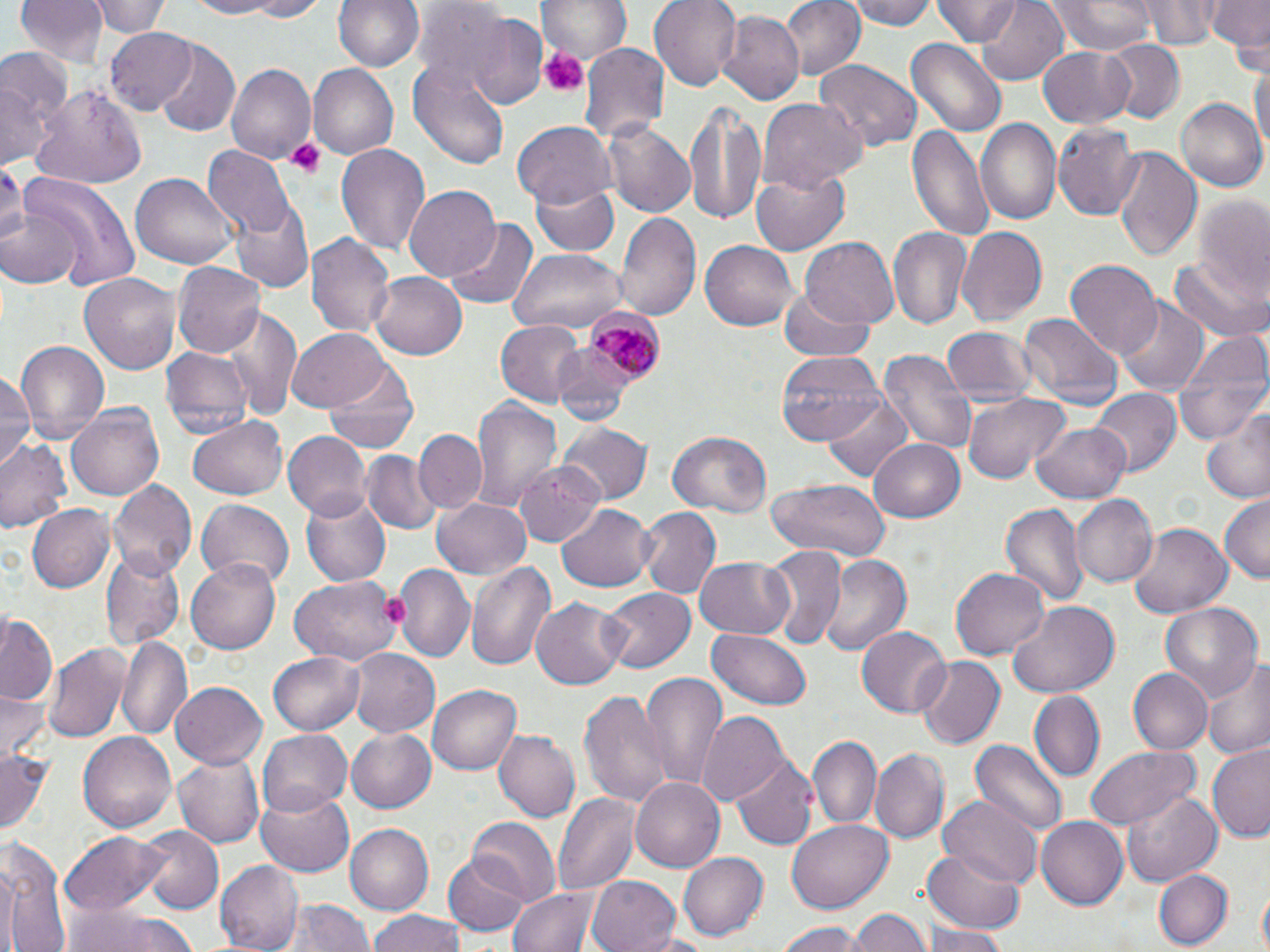

slide-level diagnosis = Plasmodium malariae
field of view = single
preparation = thin blood film
modality = optical microscopy
image size = 1270×952 pixels
magnification = 1000x
stain = May-Grünwald-Giemsa
platelet locations = approximate bounding boxes as (x1, y1, x2, y2) in pixels: (541, 48, 585, 96), (286, 137, 324, 178), (377, 591, 408, 628)
uninfected red blood cell locations = approximate bounding boxes as (x1, y1, x2, y2) in pixels: (15, 0, 111, 66), (92, 0, 167, 39), (177, 0, 292, 19), (221, 0, 336, 22), (332, 0, 425, 71), (540, 0, 629, 68), (648, 0, 742, 89), (778, 0, 864, 81), (848, 0, 938, 31), (934, 0, 1022, 46), (976, 0, 1070, 86), (1049, 0, 1158, 55), (1144, 0, 1219, 50), (1206, 0, 1268, 51), (717, 10, 805, 105), (462, 13, 547, 109), (104, 27, 199, 116), (907, 37, 1005, 137), (1103, 40, 1183, 123), (153, 43, 239, 137), (580, 43, 671, 144), (1038, 44, 1135, 128), (0, 52, 69, 168), (1249, 56, 1270, 162), (410, 61, 513, 172), (815, 61, 920, 151), (225, 63, 315, 165), (308, 64, 398, 160), (32, 84, 146, 191), (1174, 96, 1267, 193), (759, 100, 865, 190), (684, 101, 766, 225), (977, 117, 1061, 223), (512, 121, 616, 210), (603, 121, 695, 217), (1054, 121, 1143, 222), (906, 124, 992, 242), (334, 141, 432, 258), (201, 145, 293, 236), (1113, 147, 1201, 260), (0, 163, 27, 255), (753, 167, 852, 254), (131, 169, 237, 267), (22, 175, 141, 291), (529, 179, 619, 257), (404, 186, 500, 284), (1188, 191, 1270, 302), (233, 201, 314, 295), (0, 202, 83, 291), (615, 210, 702, 325), (446, 217, 537, 307), (887, 227, 972, 334), (958, 227, 1046, 326), (303, 232, 394, 338), (801, 238, 898, 330), (702, 241, 797, 328), (508, 248, 626, 334), (1172, 253, 1267, 342), (171, 260, 264, 360), (1065, 260, 1161, 358), (80, 271, 182, 374), (370, 271, 466, 360), (779, 287, 876, 361), (1116, 297, 1208, 397), (224, 311, 303, 419), (1019, 313, 1120, 406), (496, 321, 585, 407), (939, 325, 1038, 413), (289, 327, 391, 411), (1173, 330, 1269, 447), (14, 340, 110, 446), (161, 346, 252, 435), (551, 347, 637, 429), (877, 348, 976, 454), (777, 350, 886, 445), (325, 362, 420, 456), (0, 369, 36, 467), (1090, 387, 1180, 474), (822, 392, 917, 484), (962, 392, 1070, 485), (470, 398, 562, 516), (67, 403, 165, 501), (1202, 407, 1270, 504), (186, 415, 289, 500), (1030, 422, 1133, 503), (557, 423, 654, 503), (412, 429, 488, 514), (670, 430, 771, 517), (282, 431, 369, 521), (1, 438, 71, 533), (869, 438, 968, 523), (360, 451, 438, 533), (514, 460, 606, 546), (766, 477, 892, 562), (107, 479, 196, 583), (298, 489, 390, 588), (1073, 495, 1157, 586), (1220, 495, 1270, 584), (432, 498, 532, 578), (195, 499, 295, 590), (556, 503, 658, 590), (1002, 503, 1087, 607), (27, 504, 117, 593), (635, 508, 720, 598), (1127, 524, 1232, 618), (101, 547, 186, 650), (762, 547, 847, 653), (821, 556, 913, 658), (696, 557, 795, 636), (188, 559, 281, 654), (465, 560, 558, 671), (396, 566, 473, 663), (951, 566, 1050, 660), (288, 577, 398, 666), (600, 587, 693, 675), (531, 596, 626, 689), (1010, 602, 1118, 697), (1157, 602, 1264, 703), (1, 611, 61, 707), (708, 627, 812, 711), (856, 627, 951, 719), (116, 636, 191, 740), (44, 642, 130, 744), (267, 649, 366, 735), (349, 649, 439, 737), (916, 657, 1004, 750), (1205, 659, 1270, 761), (1126, 667, 1211, 755), (637, 668, 727, 790), (170, 680, 266, 769), (428, 685, 521, 777), (1, 690, 48, 764), (579, 691, 674, 807), (1029, 692, 1105, 782), (698, 711, 788, 806), (258, 729, 351, 816), (344, 729, 437, 814), (78, 730, 176, 833), (495, 731, 579, 820), (808, 734, 880, 830), (971, 738, 1068, 837), (1086, 744, 1199, 829), (1208, 746, 1270, 841), (871, 748, 947, 843), (0, 750, 54, 837), (174, 752, 265, 846), (732, 756, 819, 851), (630, 777, 723, 873), (256, 788, 355, 879), (1121, 788, 1223, 886), (553, 793, 640, 895), (939, 794, 1041, 889), (1038, 816, 1129, 911), (466, 817, 561, 906), (786, 819, 893, 913), (344, 824, 434, 916), (139, 825, 224, 914), (62, 832, 171, 913), (2, 839, 71, 952), (677, 850, 768, 941), (920, 850, 1025, 935), (443, 853, 530, 938), (216, 861, 302, 950), (1154, 871, 1230, 950), (587, 874, 682, 952), (1255, 884, 1269, 952), (508, 887, 599, 952), (272, 897, 376, 952), (63, 904, 199, 952), (848, 907, 929, 952), (366, 913, 474, 952), (776, 921, 862, 951), (925, 926, 1006, 952)
Plasmodium malariae-infected red blood cell locations = approximate bounding boxes as (x1, y1, x2, y2) in pixels: (587, 311, 667, 385)